Classify this cell by malaria status.
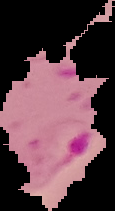
Parasitized.

Summary:
  - Image type: segmented cell region on a black background
  - Preparation: thin blood film
  - Image size: 115×211 pixels